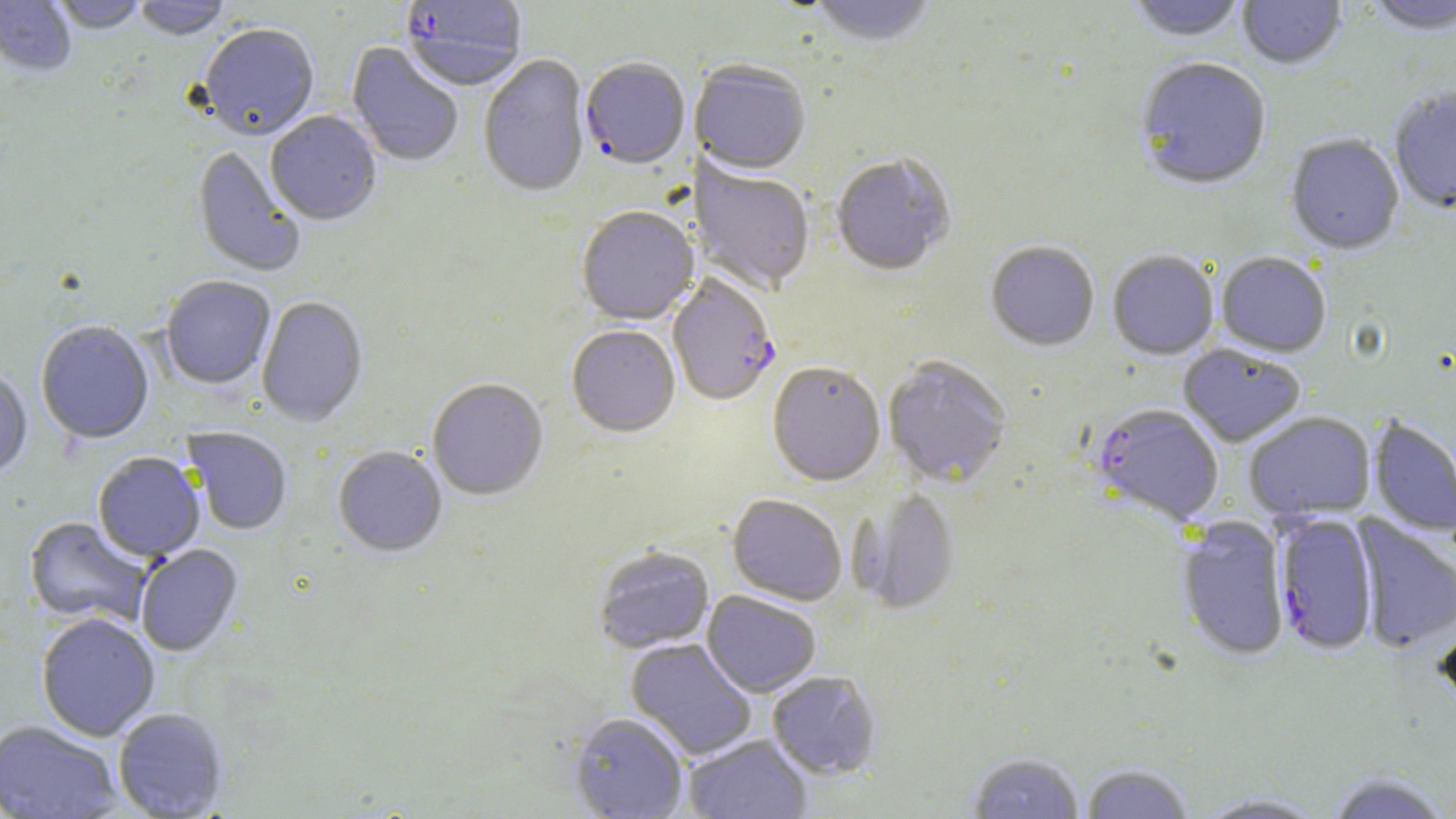
slide_level_diagnosis: Plasmodium falciparum
field_of_view: one of a larger specimen
uninfected_red_blood_cell_locations: 'approximate bounding boxes as named x1/y1/x2/y2 corners in pixels: (x1=0, y1=0, x2=76, y2=78), (x1=52, y1=0, x2=147, y2=36), (x1=134, y1=0, x2=231, y2=42), (x1=808, y1=0, x2=938, y2=49), (x1=1126, y1=0, x2=1248, y2=44), (x1=1238, y1=0, x2=1347, y2=72), (x1=1367, y1=0, x2=1456, y2=38), (x1=199, y1=25, x2=319, y2=143), (x1=346, y1=42, x2=463, y2=169), (x1=478, y1=55, x2=591, y2=200), (x1=1134, y1=60, x2=1272, y2=193), (x1=690, y1=63, x2=810, y2=178), (x1=1389, y1=89, x2=1456, y2=216), (x1=265, y1=112, x2=382, y2=227), (x1=1285, y1=135, x2=1404, y2=257), (x1=191, y1=146, x2=305, y2=278), (x1=831, y1=156, x2=955, y2=278), (x1=690, y1=157, x2=814, y2=296), (x1=576, y1=208, x2=699, y2=327), (x1=986, y1=242, x2=1099, y2=353), (x1=1107, y1=252, x2=1218, y2=361), (x1=1215, y1=253, x2=1330, y2=358), (x1=160, y1=277, x2=276, y2=390), (x1=257, y1=297, x2=368, y2=428), (x1=36, y1=322, x2=154, y2=446), (x1=566, y1=327, x2=680, y2=440), (x1=1178, y1=345, x2=1306, y2=447), (x1=884, y1=358, x2=1011, y2=489), (x1=767, y1=364, x2=886, y2=489), (x1=0, y1=372, x2=33, y2=480), (x1=427, y1=380, x2=548, y2=502), (x1=1244, y1=412, x2=1376, y2=522), (x1=1369, y1=417, x2=1456, y2=538), (x1=181, y1=427, x2=292, y2=536), (x1=333, y1=447, x2=447, y2=559), (x1=93, y1=453, x2=205, y2=563), (x1=855, y1=491, x2=961, y2=615), (x1=727, y1=495, x2=847, y2=607), (x1=1351, y1=514, x2=1456, y2=654), (x1=1176, y1=516, x2=1290, y2=662), (x1=23, y1=517, x2=152, y2=629), (x1=136, y1=545, x2=243, y2=658), (x1=593, y1=547, x2=714, y2=655), (x1=702, y1=591, x2=821, y2=698), (x1=1434, y1=613, x2=1456, y2=713), (x1=36, y1=614, x2=160, y2=742), (x1=626, y1=639, x2=757, y2=760), (x1=768, y1=671, x2=880, y2=780), (x1=113, y1=708, x2=228, y2=818), (x1=568, y1=713, x2=688, y2=818), (x1=0, y1=721, x2=123, y2=819), (x1=684, y1=734, x2=813, y2=819), (x1=968, y1=753, x2=1085, y2=819), (x1=1081, y1=765, x2=1194, y2=819), (x1=1327, y1=772, x2=1451, y2=818), (x1=1194, y1=793, x2=1331, y2=818)'
modality: optical microscopy
stain: May-Grünwald-Giemsa
magnification: 1000x
preparation: thin blood smear
image_size: 1456×819 pixels
plasmodium_falciparum_infected_red_blood_cell_locations: 'approximate bounding boxes as named x1/y1/x2/y2 corners in pixels: (x1=400, y1=0, x2=527, y2=93), (x1=580, y1=59, x2=691, y2=172), (x1=667, y1=276, x2=780, y2=408), (x1=1092, y1=405, x2=1224, y2=526), (x1=1274, y1=513, x2=1378, y2=657)'